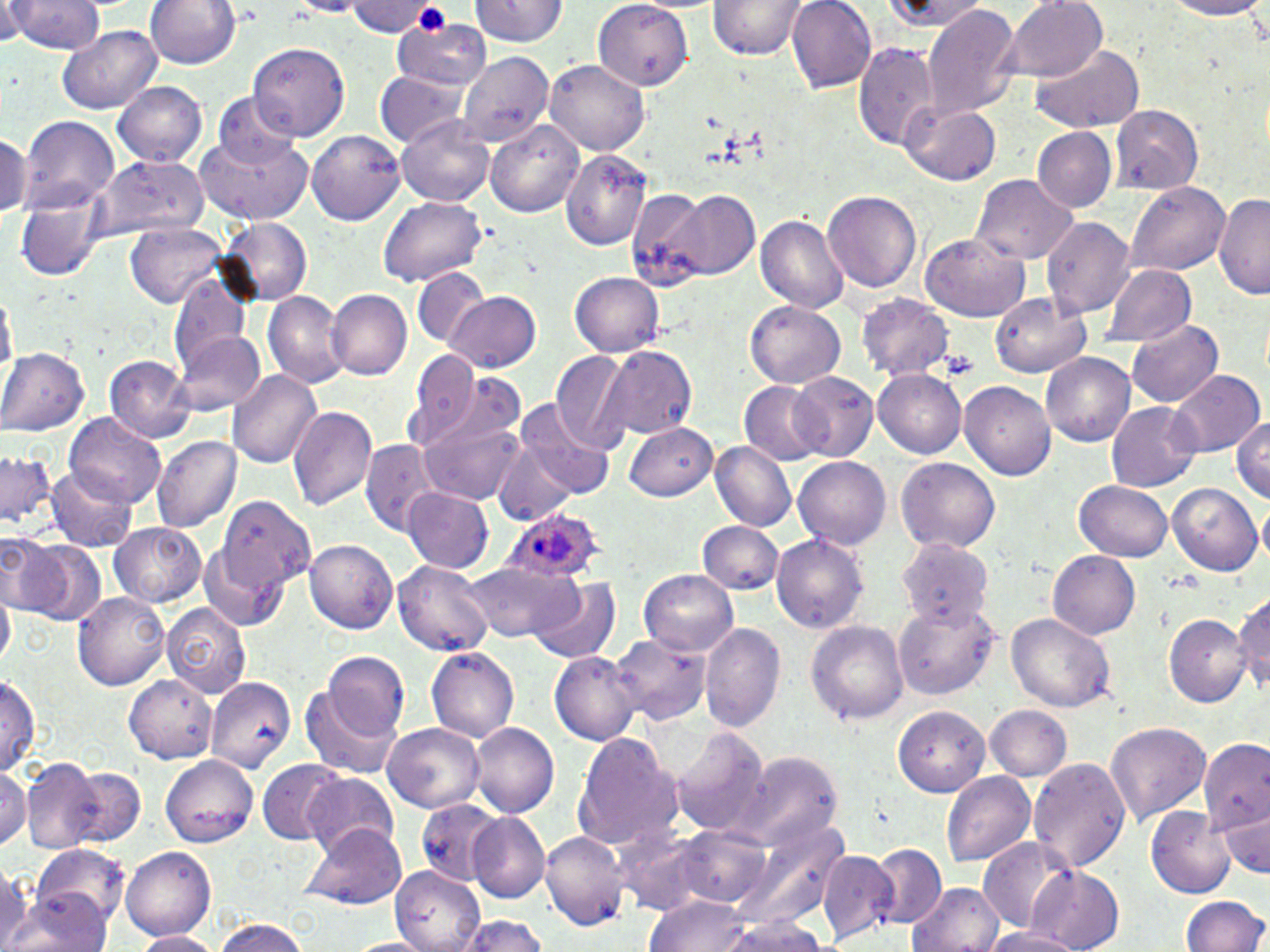

slide-level diagnosis = Plasmodium ovale
modality = light microscopy
platelet locations = approximate bounding boxes as (x1,y1)-(x2,y2) corner pairs in pixels: (940,350)-(981,383)
field of view = one of a larger specimen
Plasmodium ovale-infected red blood cell locations = approximate bounding boxes as (x1,y1)-(x2,y2) corner pairs in pixels: (505,509)-(601,583)
image size = 1270×952 pixels
preparation = thin blood smear
magnification = 1000x
stain = May-Grünwald-Giemsa
uninfected red blood cell locations = approximate bounding boxes as (x1,y1)-(x2,y2) corner pairs in pixels: (10,0)-(104,54), (143,0)-(242,70), (787,0)-(878,93), (1002,0)-(1108,83), (1156,0)-(1270,19), (1,1)-(38,46), (286,1)-(369,17), (468,1)-(570,49), (883,1)-(987,34), (345,2)-(445,37), (709,2)-(807,60), (593,3)-(689,88), (922,5)-(1022,120), (393,16)-(493,91), (57,27)-(162,112), (249,43)-(347,139), (854,43)-(940,152), (1032,45)-(1144,134), (457,51)-(552,149), (547,61)-(648,157), (375,73)-(465,151), (113,81)-(211,168), (211,93)-(307,174), (901,103)-(1003,186), (1110,106)-(1203,193), (397,115)-(497,206), (19,117)-(120,215), (486,120)-(586,217), (1032,127)-(1116,212), (194,131)-(312,223), (307,131)-(403,226), (0,132)-(28,216), (561,149)-(656,249), (95,156)-(207,243), (972,175)-(1075,264), (1125,181)-(1231,277), (822,191)-(922,294), (662,192)-(760,281), (1213,192)-(1270,299), (15,194)-(106,280), (377,197)-(486,288), (757,213)-(849,315), (219,218)-(313,304), (1044,219)-(1134,317), (125,222)-(230,308), (920,232)-(1032,320), (1103,262)-(1197,348), (411,270)-(491,351), (568,272)-(665,354), (171,278)-(251,380), (1,287)-(14,389), (327,290)-(413,381), (444,291)-(541,372), (993,291)-(1091,378), (264,293)-(345,385), (858,295)-(953,381), (745,300)-(845,387), (1128,321)-(1224,407), (172,331)-(268,417), (0,347)-(89,434), (605,347)-(696,441), (404,352)-(482,447), (105,354)-(197,443), (552,354)-(633,452), (1040,355)-(1134,447), (230,368)-(323,471), (1168,369)-(1264,456), (873,370)-(965,458), (789,373)-(878,463), (740,380)-(829,465), (959,383)-(1055,482), (515,402)-(617,499), (1107,403)-(1198,492), (288,406)-(378,512), (1232,409)-(1270,504), (418,410)-(525,505), (67,416)-(165,506), (625,423)-(715,501), (153,436)-(241,534), (360,440)-(440,534), (492,440)-(580,527), (710,442)-(796,532), (1,449)-(57,533), (794,456)-(894,549), (897,458)-(1001,553), (45,465)-(136,552), (1074,481)-(1174,562), (1167,482)-(1262,576), (404,487)-(494,575), (214,494)-(318,598), (698,521)-(783,596), (109,522)-(209,606), (773,532)-(868,637), (0,534)-(63,614), (897,537)-(996,629), (17,538)-(105,624), (305,542)-(397,634), (1049,550)-(1142,639), (394,558)-(495,657), (460,562)-(582,646), (641,569)-(738,654), (528,577)-(622,665), (1232,589)-(1270,699), (74,591)-(169,690), (894,597)-(999,702), (162,605)-(250,699), (1006,613)-(1115,712), (1167,614)-(1251,707), (807,620)-(910,725), (701,622)-(786,735), (612,635)-(707,725), (426,647)-(520,740), (549,648)-(641,744), (323,653)-(408,740), (0,673)-(39,778), (126,675)-(216,763), (207,678)-(295,774), (298,684)-(402,778), (984,705)-(1070,783), (896,706)-(991,795), (383,722)-(486,812), (471,723)-(560,818), (1106,723)-(1210,825), (672,727)-(770,838), (572,731)-(681,851), (1203,736)-(1268,838), (163,755)-(258,847), (742,755)-(840,851), (1028,755)-(1134,872), (258,759)-(347,843), (21,762)-(103,853), (0,766)-(28,848), (59,767)-(146,851), (943,771)-(1035,869), (302,775)-(401,860), (414,798)-(503,889), (1148,805)-(1235,899), (1214,806)-(1270,880), (472,811)-(548,902), (300,822)-(408,909), (671,824)-(774,911), (540,830)-(627,931), (978,836)-(1076,933), (866,843)-(945,925), (122,844)-(216,940), (33,845)-(131,927), (818,852)-(897,941), (394,864)-(486,951), (1027,864)-(1126,952), (0,867)-(33,947), (909,881)-(1004,952), (3,890)-(111,952), (1182,896)-(1268,952), (644,897)-(761,952), (451,915)-(554,952), (718,917)-(833,952), (210,920)-(314,952), (984,927)-(1084,952), (133,930)-(219,952)